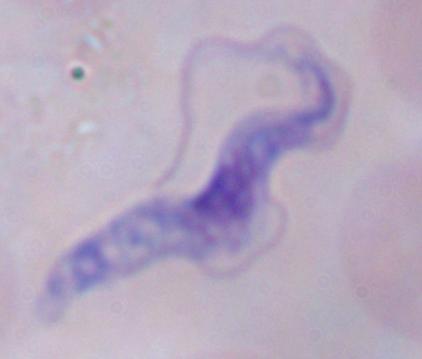

Summary:
  - Identification: trypanosome
  - Magnification: 1000x
  - Modality: micrograph